Identify the parasite.
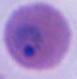
Plasmodium.

Summary:
  - Modality: photomicrograph
  - Magnification: 400x or 1000x